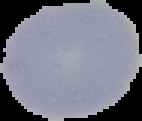 From a thin blood smear. Cell region segmented out of the field of view; the surrounding area is masked to black. Image is 142×121 pixels. Result: negative for Plasmodium parasites.